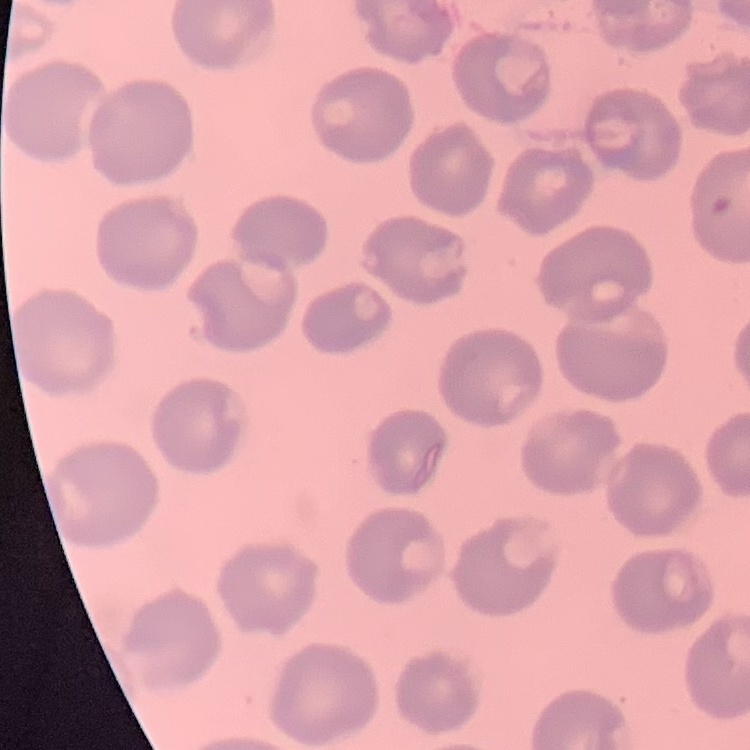
Summary:
  - Red blood cell morphology: no rouleaux formation
  - Stain: Field's or Giemsa
  - Preparation: thin blood film
  - Image type: one tile cut from a larger photomicrograph